Describe the morphology of the red blood cells.
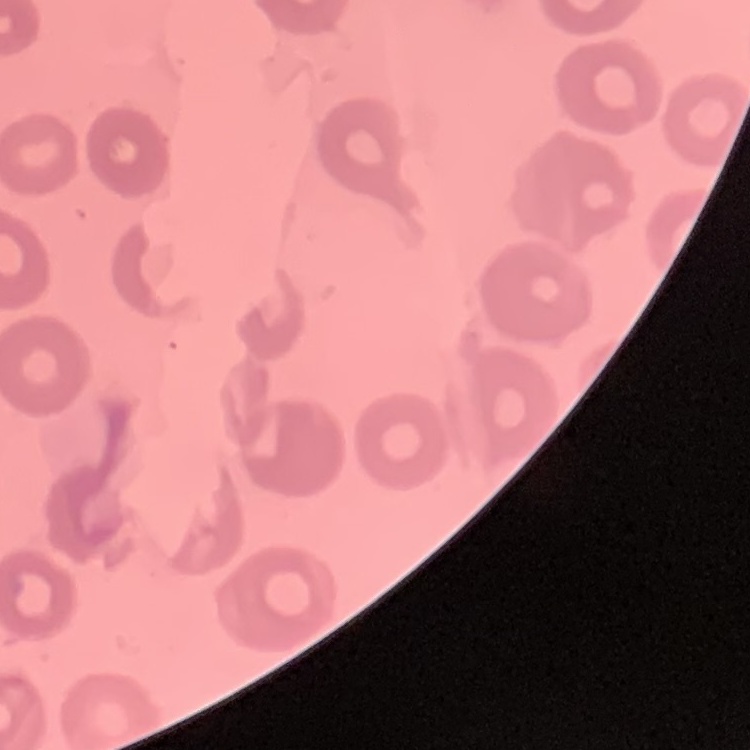
No rouleaux formation.

One tile cut from a larger photomicrograph. Stained with either Field's or Giemsa. Thin blood film.